Assess this cell for malaria.
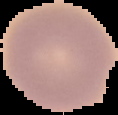

It is uninfected.

Image is 118×115 pixels. From a thin blood smear. Segmented cell region on a black background.